Locate every blood parasite and identify its species.
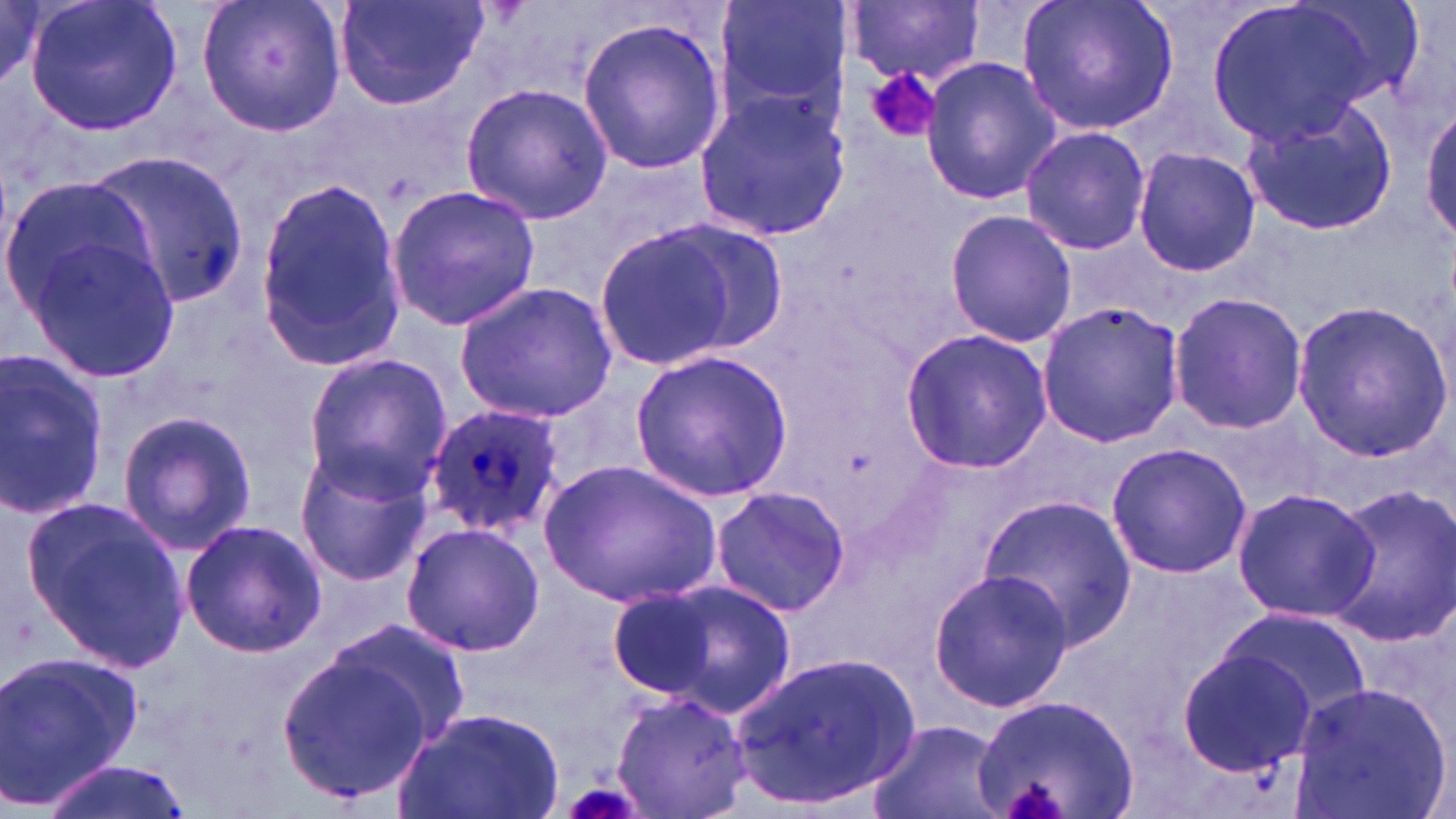
Approximate bounding boxes as named x1/y1/x2/y2 corners in pixels.
Plasmodium ovale-infected red blood cells: (x1=423, y1=400, x2=565, y2=537).
No Plasmodium falciparum, Plasmodium malariae, Plasmodium vivax, Babesia divergens, or Trypanosoma brucei observed.

slide-level diagnosis = Plasmodium ovale
platelet locations = approximate bounding boxes as named x1/y1/x2/y2 corners in pixels: (x1=863, y1=64, x2=942, y2=144), (x1=1003, y1=783, x2=1067, y2=819), (x1=564, y1=787, x2=640, y2=819)
image size = 1456×819 pixels
stain = May-Grünwald-Giemsa
uninfected red blood cell locations = approximate bounding boxes as named x1/y1/x2/y2 corners in pixels: (x1=24, y1=0, x2=184, y2=137), (x1=196, y1=0, x2=347, y2=139), (x1=332, y1=0, x2=492, y2=112), (x1=713, y1=0, x2=852, y2=136), (x1=1018, y1=0, x2=1179, y2=136), (x1=848, y1=1, x2=984, y2=84), (x1=1203, y1=2, x2=1384, y2=146), (x1=575, y1=14, x2=728, y2=177), (x1=919, y1=57, x2=1062, y2=205), (x1=460, y1=82, x2=612, y2=226), (x1=693, y1=90, x2=850, y2=242), (x1=1242, y1=98, x2=1399, y2=237), (x1=1421, y1=101, x2=1456, y2=247), (x1=1018, y1=126, x2=1150, y2=253), (x1=1133, y1=145, x2=1259, y2=277), (x1=88, y1=149, x2=248, y2=312), (x1=0, y1=172, x2=163, y2=333), (x1=255, y1=183, x2=407, y2=368), (x1=386, y1=184, x2=540, y2=331), (x1=946, y1=207, x2=1076, y2=348), (x1=587, y1=221, x2=766, y2=373), (x1=23, y1=228, x2=181, y2=384), (x1=454, y1=279, x2=617, y2=423), (x1=1168, y1=293, x2=1309, y2=436), (x1=1036, y1=300, x2=1185, y2=449), (x1=1289, y1=300, x2=1450, y2=459), (x1=899, y1=329, x2=1052, y2=473), (x1=630, y1=350, x2=793, y2=501), (x1=0, y1=352, x2=109, y2=518), (x1=300, y1=352, x2=451, y2=496), (x1=117, y1=411, x2=260, y2=556), (x1=1104, y1=442, x2=1253, y2=578), (x1=290, y1=443, x2=435, y2=586), (x1=541, y1=459, x2=721, y2=609), (x1=709, y1=485, x2=852, y2=615), (x1=1230, y1=485, x2=1378, y2=624), (x1=1322, y1=486, x2=1456, y2=649), (x1=978, y1=491, x2=1138, y2=653), (x1=22, y1=497, x2=190, y2=668), (x1=178, y1=518, x2=329, y2=661), (x1=398, y1=520, x2=548, y2=659), (x1=927, y1=567, x2=1073, y2=713), (x1=622, y1=575, x2=801, y2=718), (x1=1219, y1=609, x2=1370, y2=723), (x1=320, y1=616, x2=472, y2=748), (x1=276, y1=643, x2=445, y2=803), (x1=1179, y1=648, x2=1315, y2=776), (x1=0, y1=650, x2=140, y2=809), (x1=732, y1=651, x2=921, y2=809), (x1=1287, y1=681, x2=1452, y2=819), (x1=610, y1=684, x2=751, y2=818), (x1=971, y1=692, x2=1140, y2=819), (x1=389, y1=703, x2=567, y2=819), (x1=868, y1=718, x2=1008, y2=819), (x1=39, y1=755, x2=196, y2=819)
modality = light microscopy
magnification = 1000x
preparation = thin blood film
field of view = one of a larger specimen